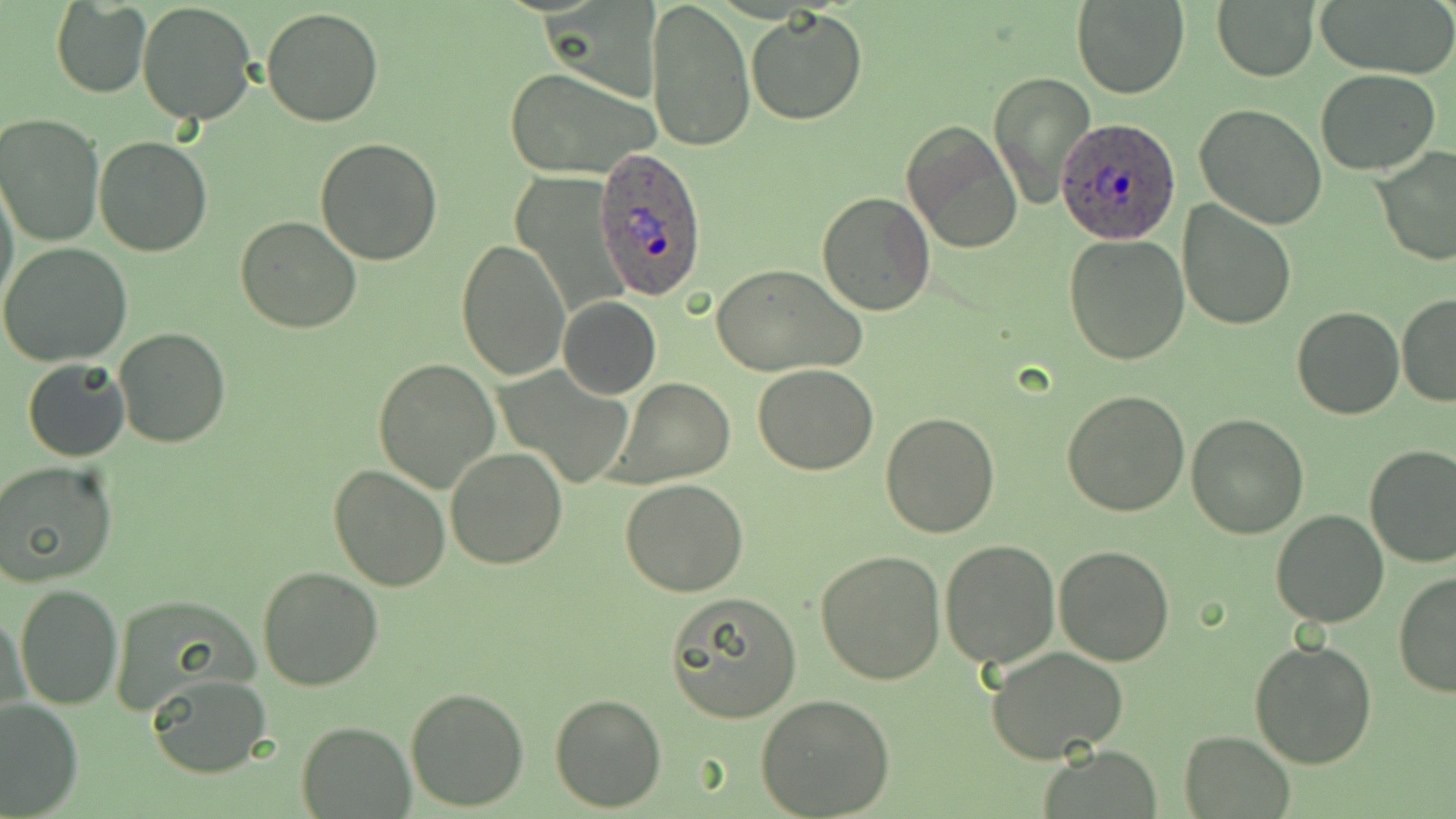 Approximate bounding boxes as named x1/y1/x2/y2 corners in pixels. Plasmodium ovale-infected red blood cell locations: (x1=1058, y1=117, x2=1179, y2=245), (x1=592, y1=147, x2=707, y2=301). Uninfected red blood cell locations: (x1=544, y1=0, x2=659, y2=103), (x1=646, y1=0, x2=754, y2=152), (x1=1073, y1=0, x2=1188, y2=98), (x1=1313, y1=0, x2=1455, y2=79), (x1=51, y1=2, x2=151, y2=97), (x1=137, y1=2, x2=258, y2=126), (x1=1213, y1=3, x2=1318, y2=80), (x1=261, y1=8, x2=384, y2=126), (x1=744, y1=8, x2=869, y2=126), (x1=503, y1=67, x2=661, y2=180), (x1=1316, y1=70, x2=1441, y2=174), (x1=987, y1=71, x2=1095, y2=208), (x1=1195, y1=105, x2=1329, y2=228), (x1=0, y1=112, x2=104, y2=247), (x1=902, y1=121, x2=1022, y2=254), (x1=95, y1=137, x2=212, y2=257), (x1=315, y1=137, x2=442, y2=265), (x1=1374, y1=146, x2=1456, y2=266), (x1=0, y1=177, x2=19, y2=314), (x1=817, y1=191, x2=936, y2=315), (x1=1176, y1=200, x2=1298, y2=332), (x1=235, y1=215, x2=362, y2=333), (x1=1063, y1=234, x2=1190, y2=365), (x1=458, y1=236, x2=570, y2=379), (x1=0, y1=243, x2=133, y2=368), (x1=710, y1=263, x2=868, y2=377), (x1=1396, y1=293, x2=1455, y2=407), (x1=558, y1=297, x2=661, y2=399), (x1=1293, y1=305, x2=1405, y2=419), (x1=115, y1=326, x2=231, y2=447), (x1=372, y1=358, x2=501, y2=493), (x1=22, y1=359, x2=130, y2=462), (x1=753, y1=363, x2=877, y2=475), (x1=499, y1=366, x2=636, y2=488), (x1=611, y1=378, x2=736, y2=487), (x1=1060, y1=389, x2=1190, y2=518), (x1=881, y1=411, x2=1000, y2=538), (x1=1186, y1=414, x2=1307, y2=537), (x1=1363, y1=444, x2=1456, y2=567), (x1=445, y1=446, x2=566, y2=569), (x1=0, y1=461, x2=120, y2=586), (x1=328, y1=464, x2=451, y2=591), (x1=620, y1=478, x2=749, y2=596), (x1=1270, y1=509, x2=1392, y2=628), (x1=939, y1=539, x2=1061, y2=668), (x1=1053, y1=544, x2=1178, y2=666), (x1=816, y1=550, x2=947, y2=685), (x1=256, y1=566, x2=384, y2=690), (x1=1394, y1=572, x2=1456, y2=697), (x1=14, y1=583, x2=121, y2=709), (x1=667, y1=592, x2=802, y2=722), (x1=107, y1=593, x2=259, y2=715), (x1=3, y1=604, x2=28, y2=726), (x1=1249, y1=640, x2=1377, y2=770), (x1=985, y1=645, x2=1133, y2=767), (x1=145, y1=673, x2=271, y2=779), (x1=404, y1=687, x2=529, y2=811), (x1=550, y1=691, x2=667, y2=811), (x1=755, y1=693, x2=896, y2=817), (x1=0, y1=699, x2=83, y2=816), (x1=296, y1=722, x2=415, y2=818), (x1=1179, y1=731, x2=1294, y2=818), (x1=1038, y1=745, x2=1165, y2=819). Slide-level diagnosis: Plasmodium ovale. Image is 1456×819 pixels. Single field of view. May-Grünwald-Giemsa stain. Optical microscopy. Thin blood smear. Captured at 1000x magnification.